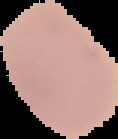
Summary:
  - Preparation: thin blood film
  - Image type: segmented cell region with the area outside set to black
  - Malaria status: uninfected
  - Image size: 118×139 pixels